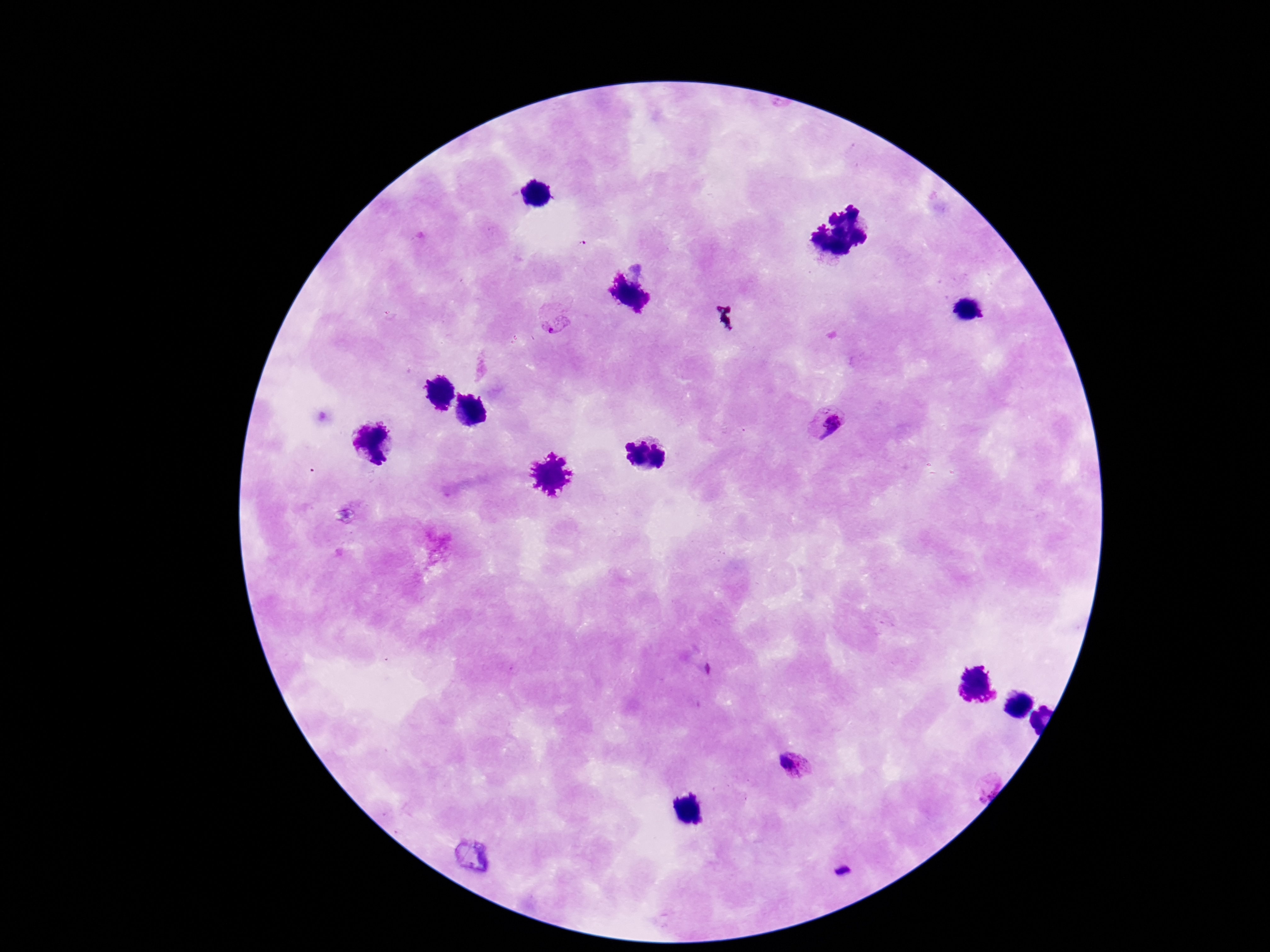

{
  "stain": "Giemsa",
  "patient_malaria_status": "positive",
  "image_size": "1270×952 pixels",
  "capture": "smartphone camera through the microscope eyepiece",
  "plasmodium_parasite_locations": "approximate centers as {x, y} in pixels: {557, 326}, {828, 422}, {798, 762}, {985, 786}",
  "field_of_view": "single",
  "magnification": "100x",
  "preparation": "thick blood smear"
}